Classify this cell by malaria status.
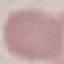
It is uninfected.

preparation: thin blood film
capture: smartphone through the microscope eyepiece
stain: Giemsa
image_type: automatically extracted cell patch, resized to 64 × 64 pixels